Locate every blood parasite and identify its species.
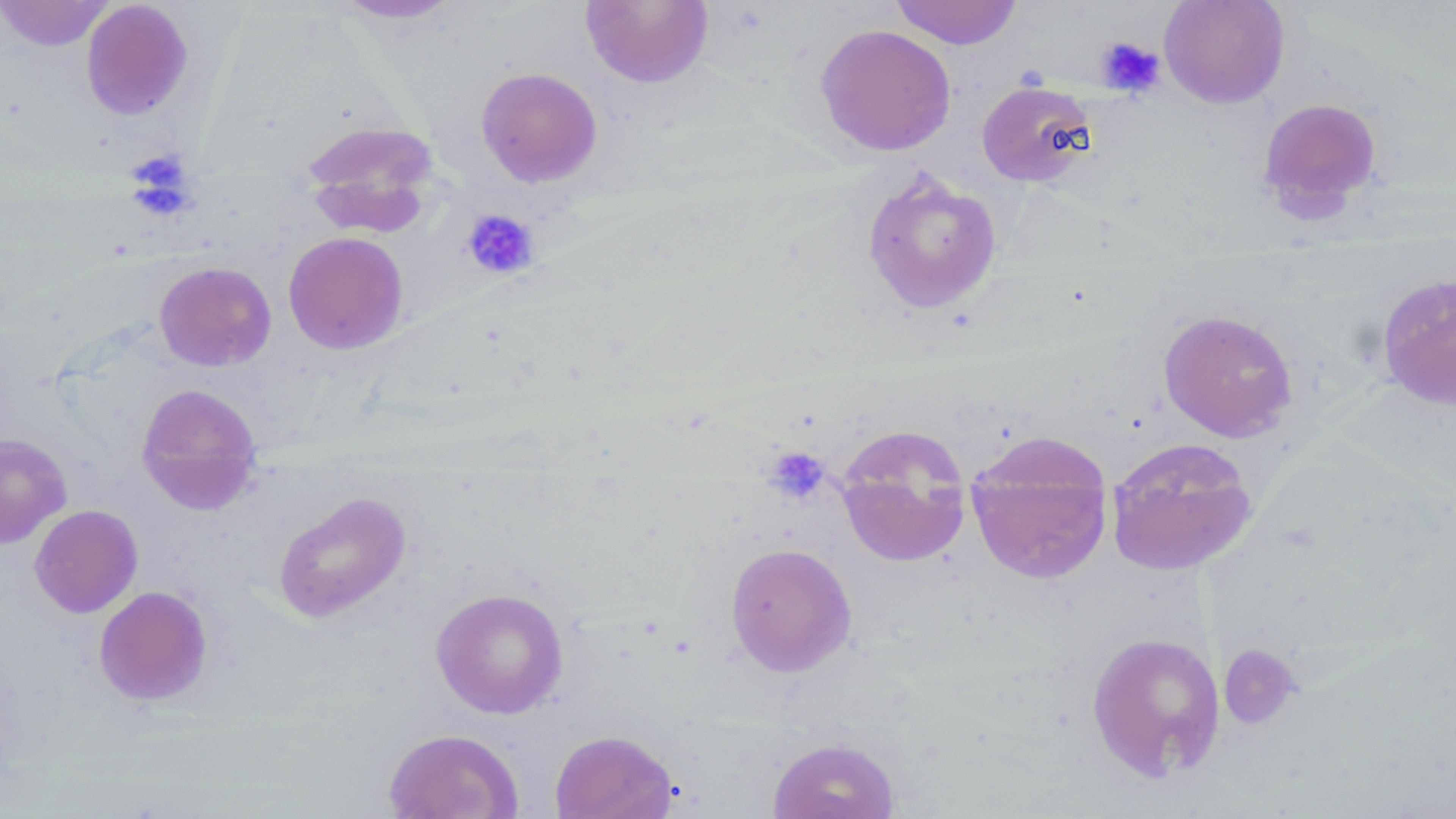

No blood parasites observed.

Approximate bounding boxes as named x1/y1/x2/y2 corners in pixels. Uninfected red blood cell locations: (x1=0, y1=0, x2=115, y2=51), (x1=331, y1=0, x2=464, y2=24), (x1=580, y1=0, x2=713, y2=88), (x1=890, y1=0, x2=1022, y2=49), (x1=1158, y1=0, x2=1290, y2=108), (x1=80, y1=1, x2=194, y2=120), (x1=814, y1=24, x2=957, y2=156), (x1=476, y1=67, x2=603, y2=187), (x1=977, y1=80, x2=1096, y2=187), (x1=1256, y1=96, x2=1383, y2=222), (x1=301, y1=120, x2=439, y2=231), (x1=861, y1=170, x2=1002, y2=314), (x1=283, y1=231, x2=409, y2=354), (x1=154, y1=261, x2=276, y2=371), (x1=1376, y1=272, x2=1456, y2=411), (x1=1158, y1=308, x2=1297, y2=442), (x1=136, y1=383, x2=263, y2=514), (x1=835, y1=425, x2=973, y2=568), (x1=965, y1=430, x2=1115, y2=585), (x1=0, y1=433, x2=72, y2=548), (x1=1105, y1=437, x2=1258, y2=576), (x1=273, y1=491, x2=412, y2=623), (x1=29, y1=504, x2=143, y2=618), (x1=724, y1=541, x2=857, y2=677), (x1=94, y1=586, x2=213, y2=706), (x1=430, y1=587, x2=569, y2=719), (x1=1086, y1=630, x2=1225, y2=782), (x1=1218, y1=643, x2=1300, y2=730), (x1=383, y1=729, x2=524, y2=818), (x1=549, y1=729, x2=678, y2=819), (x1=767, y1=736, x2=900, y2=819). Platelet locations: (x1=1095, y1=36, x2=1164, y2=97), (x1=125, y1=151, x2=196, y2=217), (x1=462, y1=208, x2=539, y2=280), (x1=764, y1=446, x2=831, y2=504). Slide-level diagnosis: negative for blood parasites. 1000x magnification. Thin blood film. Image is 1456×819 pixels. May-Grünwald-Giemsa-stained preparation. Light microscopy. One field of a larger specimen.